Identify the parasite.
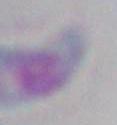

Toxoplasma gondii.

magnification = 1000x
modality = photomicrograph